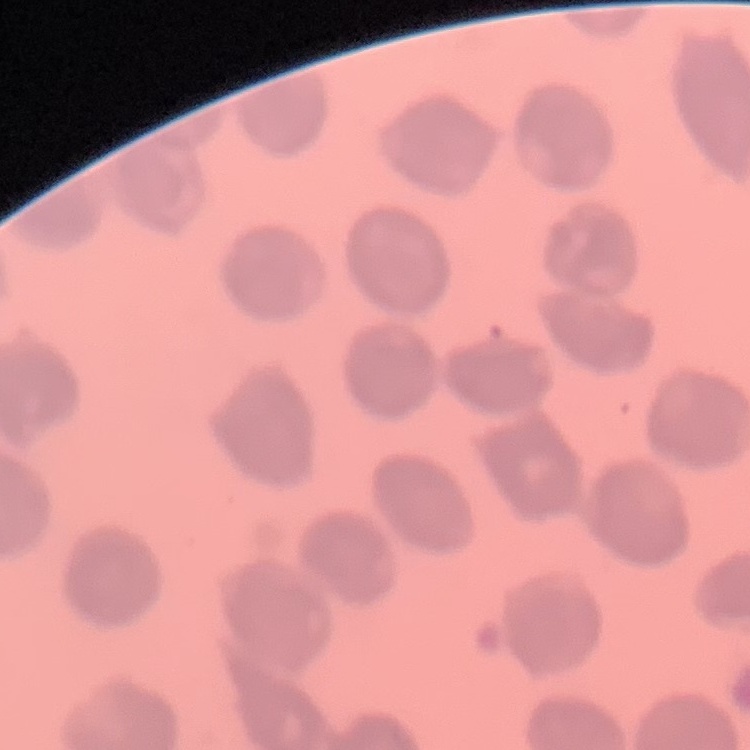

Summary:
  - Erythrocyte morphology: no rouleaux formation
  - Stain: Field's or Giemsa
  - Image type: square crop of a larger photomicrograph
  - Preparation: thin blood smear